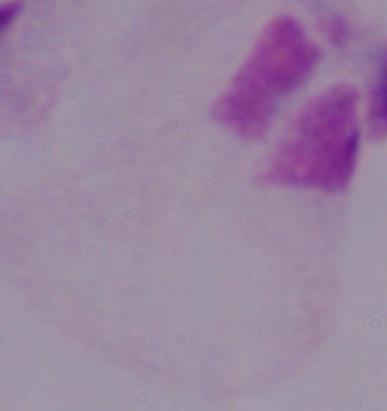
Photomicrograph. A trichomonad is seen. Captured at 1000x magnification.